Give the preparation type.
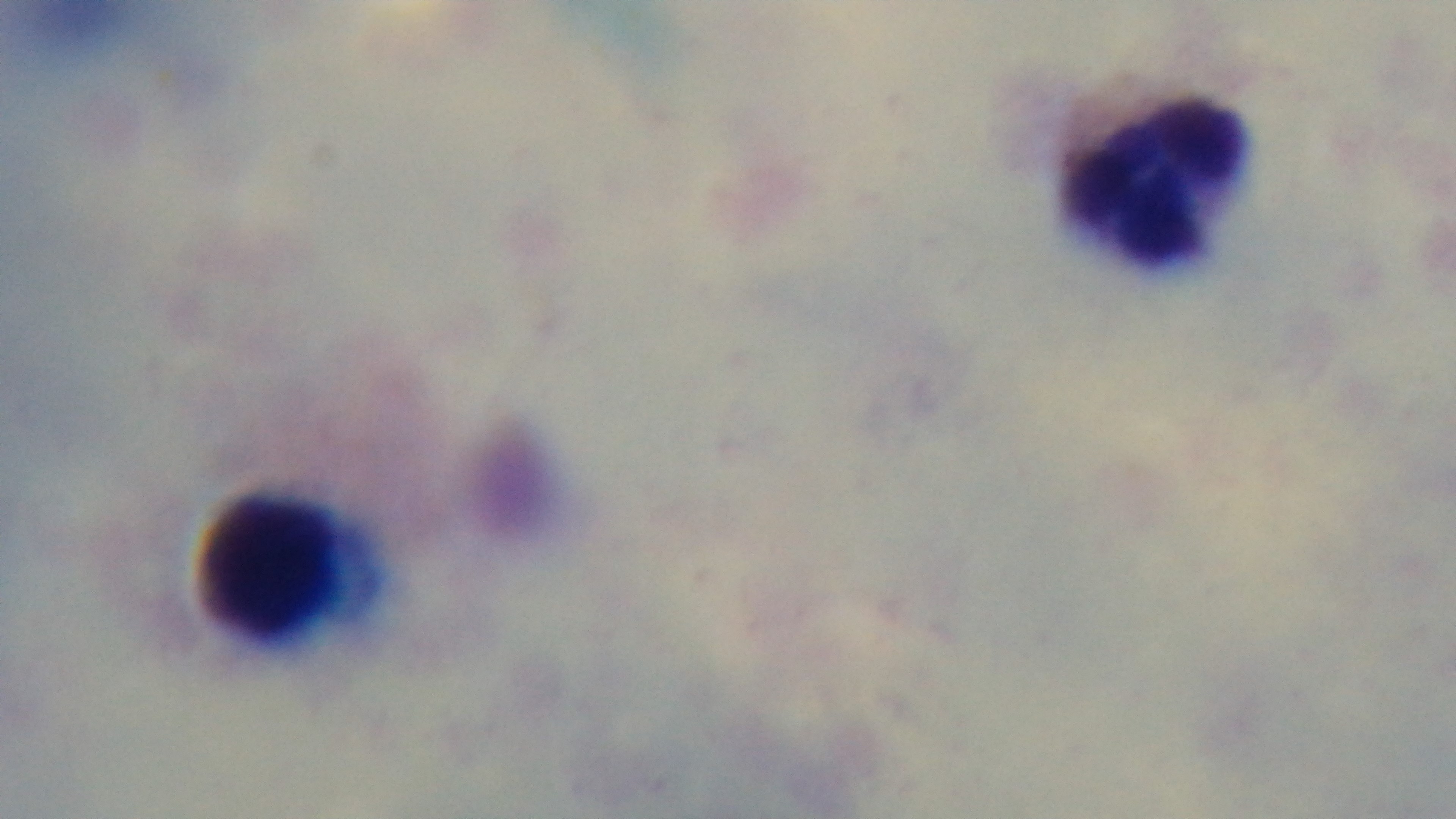

It is a thick blood film.

100x oil-immersion objective. Giemsa stain. Light microscopy. Captured with a mounted 4K digital camera. One field from the slide. Malaria status: uninfected.